Classify this cell by malaria status.
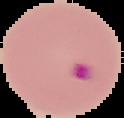
Parasitized.

From a thin blood film. Image is 124×118 pixels. Segmented cell region on a black background.